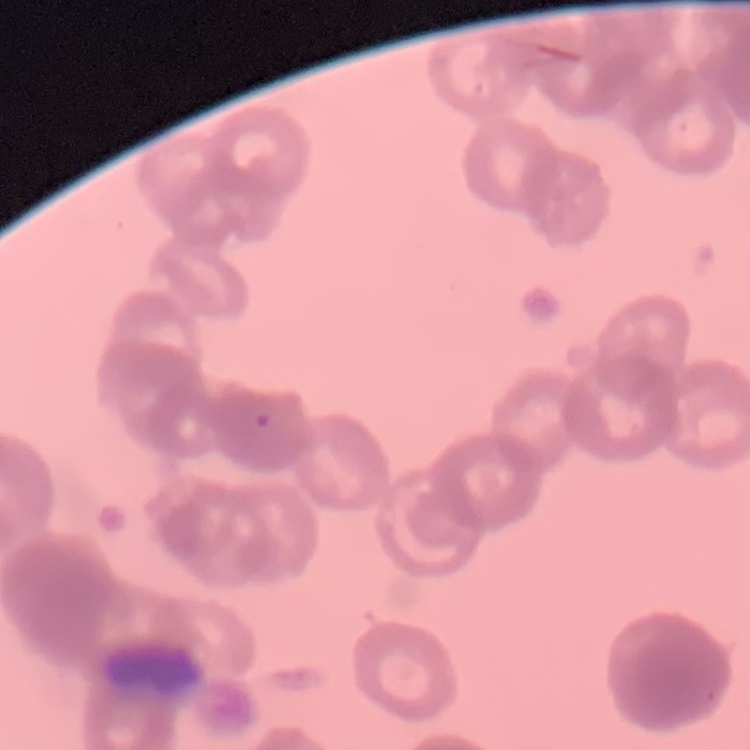

Summary:
  - Red blood cell morphology: rouleaux formation
  - Stain: Field's or Giemsa
  - Preparation: thin blood film
  - Image type: one tile cut from a larger photomicrograph